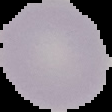

Image is 112×112 pixels. The area outside the segmented cell region is set to black. Result: no Plasmodium parasites detected. From a thin blood film.